Give the location of every parasitized RBC.
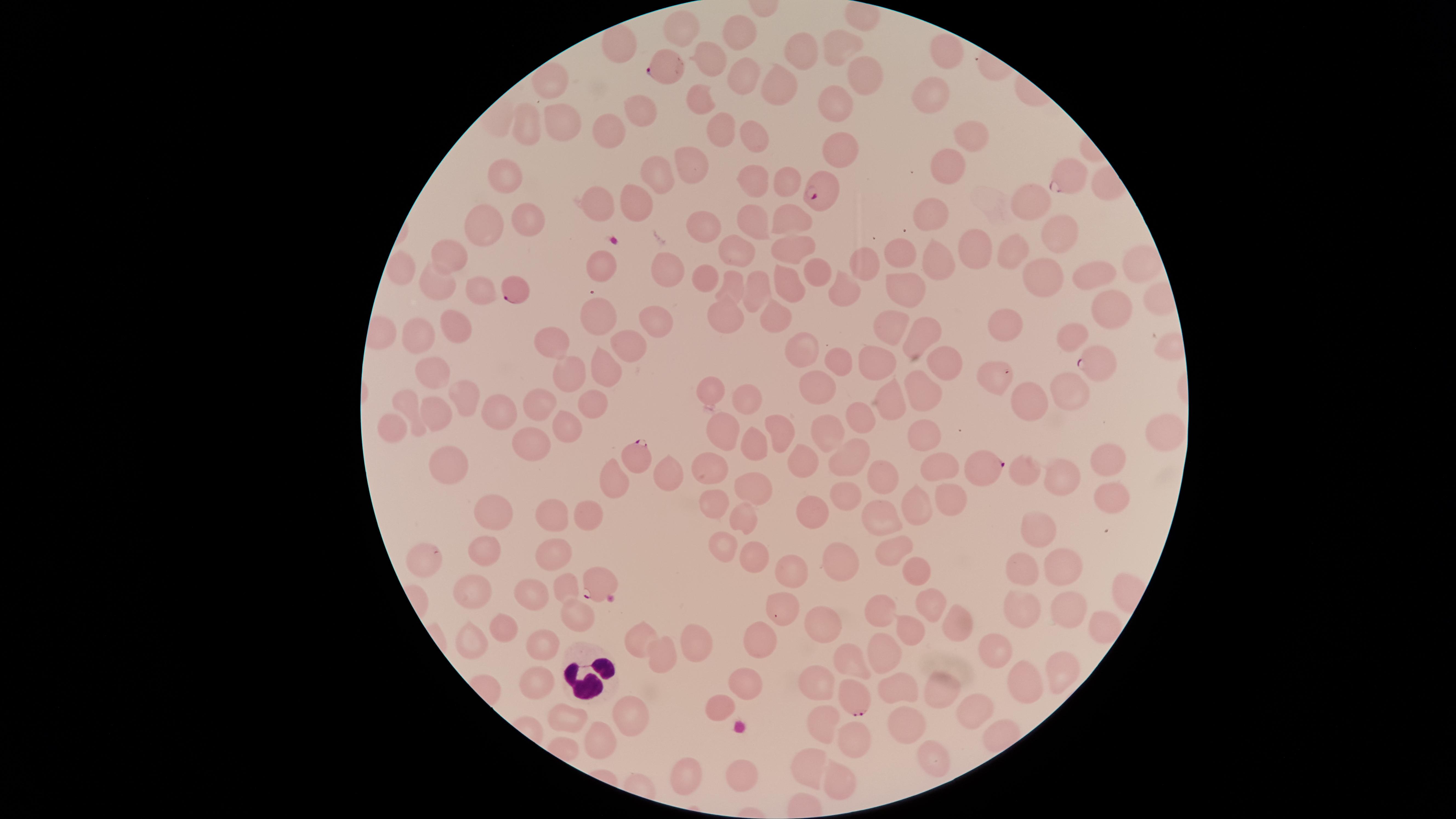

Approximate marker points, in pixels from the top-left corner.
Parasitized RBCs: (x=661, y=68), (x=1070, y=177), (x=826, y=189), (x=516, y=289), (x=1103, y=361), (x=645, y=457), (x=989, y=462), (x=601, y=579), (x=854, y=700).

uninfected RBCs = approximate marker points, in pixels from the top-left corner: (x=683, y=32), (x=734, y=32), (x=623, y=42), (x=837, y=46), (x=806, y=54), (x=954, y=56), (x=708, y=58), (x=859, y=76), (x=734, y=77), (x=550, y=84), (x=776, y=87), (x=935, y=92), (x=700, y=102), (x=832, y=102), (x=637, y=112), (x=561, y=118), (x=525, y=123), (x=611, y=129), (x=717, y=131), (x=970, y=133), (x=750, y=143), (x=840, y=151), (x=952, y=164), (x=693, y=166), (x=508, y=168), (x=653, y=174), (x=788, y=177), (x=748, y=180), (x=1029, y=201), (x=597, y=203), (x=636, y=203), (x=931, y=213), (x=531, y=216), (x=483, y=218), (x=748, y=219), (x=785, y=220), (x=702, y=225), (x=1058, y=227), (x=983, y=245), (x=736, y=246), (x=794, y=247), (x=1022, y=251), (x=448, y=253), (x=895, y=255), (x=947, y=258), (x=1138, y=264), (x=866, y=266), (x=820, y=267), (x=666, y=269), (x=597, y=271), (x=1100, y=273), (x=709, y=276), (x=1046, y=279), (x=433, y=283), (x=792, y=283), (x=730, y=284), (x=756, y=287), (x=475, y=288), (x=900, y=289), (x=841, y=293), (x=1111, y=304), (x=724, y=309), (x=776, y=312), (x=599, y=313), (x=651, y=315), (x=890, y=320), (x=451, y=325), (x=1008, y=325), (x=928, y=333), (x=1075, y=333), (x=420, y=334), (x=552, y=341), (x=636, y=341), (x=810, y=344), (x=838, y=360), (x=878, y=360), (x=603, y=364), (x=941, y=364), (x=571, y=370), (x=433, y=374), (x=994, y=374), (x=1068, y=382), (x=816, y=386), (x=921, y=390), (x=712, y=393), (x=1030, y=393), (x=466, y=398), (x=741, y=398), (x=889, y=402), (x=592, y=404), (x=538, y=406), (x=410, y=408), (x=439, y=408), (x=498, y=415), (x=860, y=421), (x=392, y=423), (x=567, y=423), (x=782, y=427), (x=1164, y=430), (x=924, y=432), (x=723, y=435), (x=825, y=435), (x=529, y=444), (x=753, y=445), (x=844, y=455), (x=1110, y=458), (x=450, y=462), (x=808, y=462), (x=942, y=463), (x=714, y=468), (x=669, y=471), (x=1033, y=475), (x=881, y=476), (x=609, y=481), (x=1062, y=481), (x=757, y=484), (x=846, y=491), (x=1111, y=491), (x=945, y=498), (x=714, y=504), (x=493, y=505), (x=812, y=508), (x=914, y=510), (x=591, y=512), (x=745, y=513), (x=875, y=516), (x=551, y=518), (x=1041, y=529), (x=897, y=550), (x=481, y=552), (x=722, y=552), (x=424, y=556), (x=555, y=557), (x=753, y=557), (x=841, y=562), (x=1072, y=562), (x=790, y=570), (x=1032, y=570), (x=915, y=572), (x=475, y=588), (x=568, y=588), (x=531, y=599), (x=932, y=599), (x=1027, y=607), (x=1069, y=611), (x=572, y=615), (x=785, y=616), (x=882, y=617), (x=955, y=617), (x=1098, y=623), (x=826, y=627), (x=500, y=630), (x=912, y=635), (x=641, y=637), (x=470, y=643), (x=540, y=643), (x=760, y=643), (x=698, y=644), (x=883, y=649), (x=990, y=649), (x=662, y=658), (x=852, y=665), (x=1058, y=671), (x=532, y=678), (x=1029, y=678), (x=748, y=679), (x=821, y=684), (x=937, y=689), (x=896, y=690), (x=721, y=707), (x=979, y=711), (x=631, y=715), (x=562, y=716), (x=820, y=725), (x=906, y=725), (x=599, y=740), (x=850, y=746), (x=927, y=757), (x=810, y=765), (x=738, y=776), (x=678, y=777), (x=842, y=780)
preparation = thin smear of blood
stain = Giemsa
field of view = single
WBCs = approximate marker points, in pixels from the top-left corner: (x=594, y=681)
capture = smartphone photograph through the microscope eyepiece
visible region = circular
image size = 1456×819 pixels
species = Plasmodium falciparum